Assess this cell for malaria.
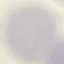

It is uninfected.

capture: smartphone through the microscope eyepiece
stain: Giemsa
image_type: cell patch, automatically extracted from a larger field of view and resized to 64 × 64 pixels
preparation: thin blood smear